Report the malaria status of this cell.
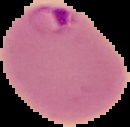
Parasitized.

Image is 130×127 pixels. The area outside the segmented cell region is set to black. From a thin blood smear.